Locate every malaria parasite.
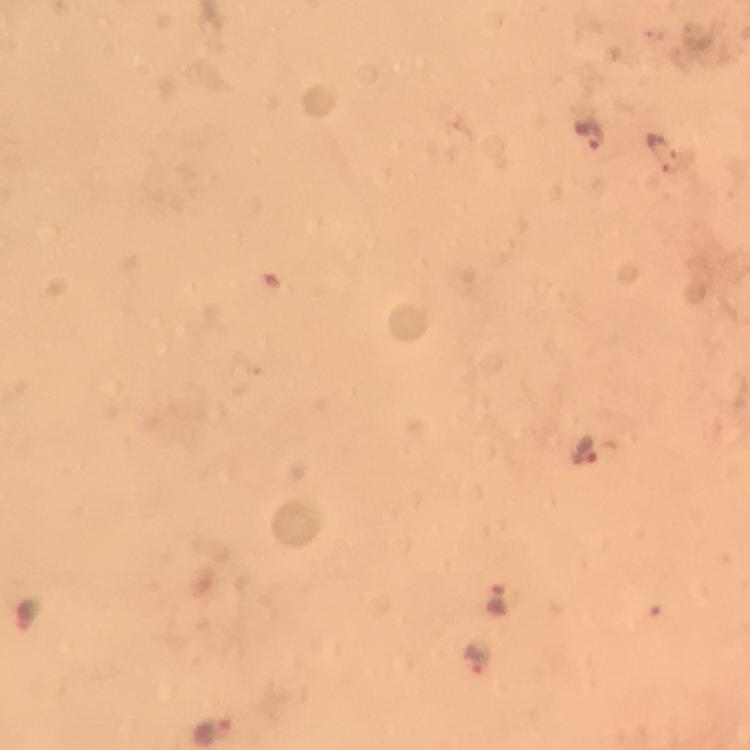

Approximate centers as (x, y) in pixels.
Malaria parasites: (589, 133), (665, 149), (587, 448), (501, 598), (477, 657).

A crop from one field of view. Immersion oil applied. Image is 750×750 pixels. At 100x magnification. Giemsa stain. Photographed with a smartphone mounted on the microscope. From a malaria diagnostic workup. Thick blood smear.